Assess the morphology of the red blood cells.
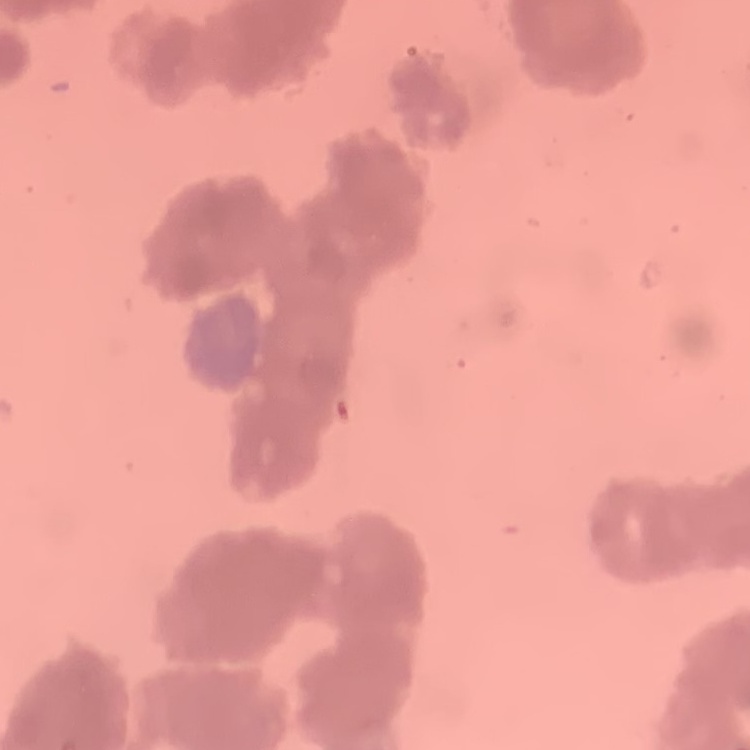
Rouleaux formation.

stain: Field's or Giemsa
preparation: thin blood film
image_type: one tile cut from a larger photomicrograph